Identify the preparation type.
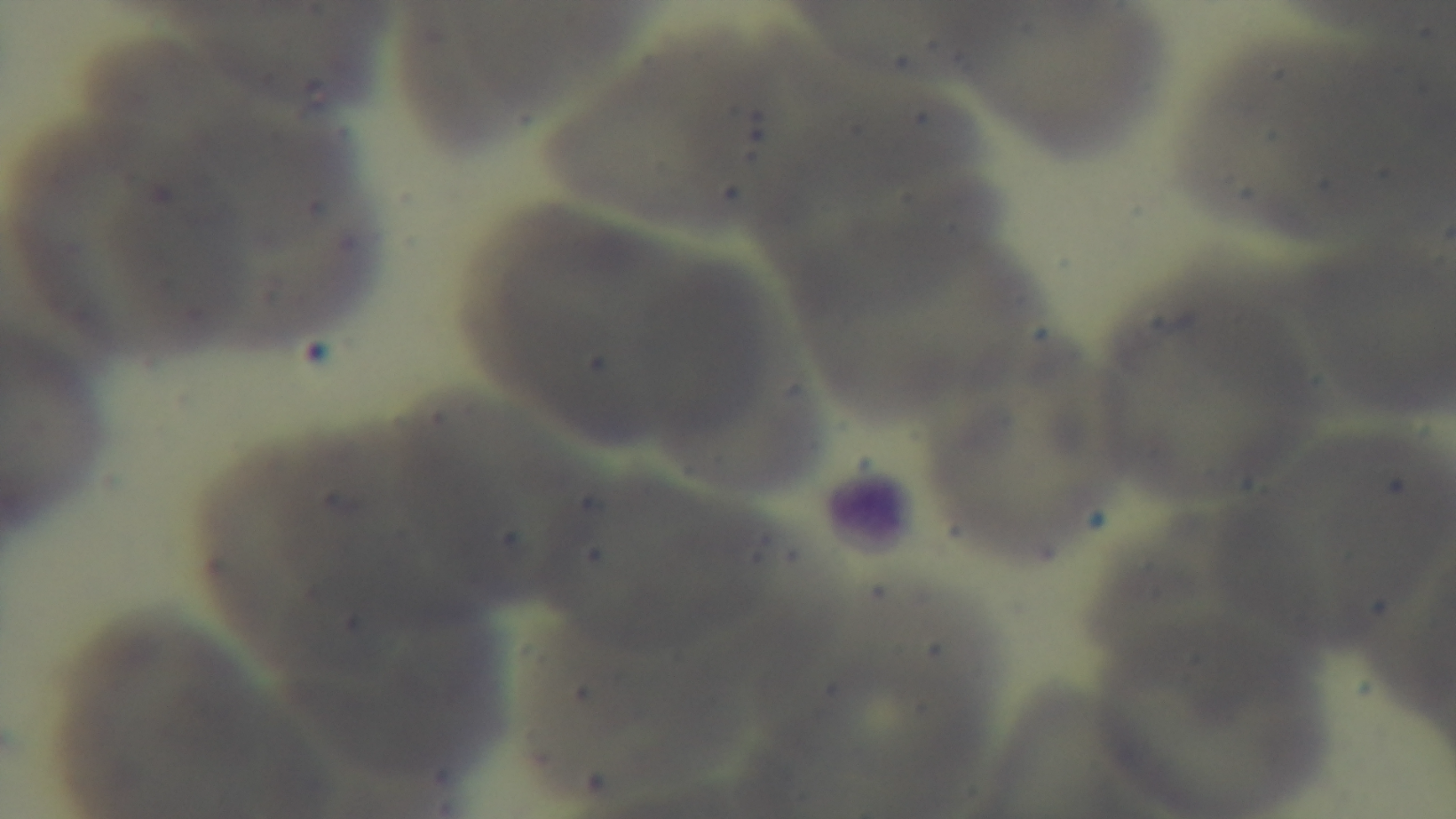

Thin.

field of view = one from the slide
objective = 100x oil immersion
capture = mounted 4K digital camera
malaria status = uninfected
modality = light microscopy
stain = Giemsa